Report the malaria status of this cell.
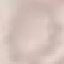

It is uninfected.

Summary:
  - Capture: smartphone through the microscope eyepiece
  - Image type: automatically extracted cell patch, resized to 64 × 64 pixels
  - Stain: Giemsa
  - Preparation: thin blood smear